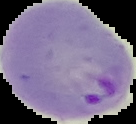

From a thin blood smear. The area outside the segmented cell region is set to black. Image is 136×124 pixels. Result: malaria parasites identified.